Locate every Plasmodium malariae-infected red blood cell.
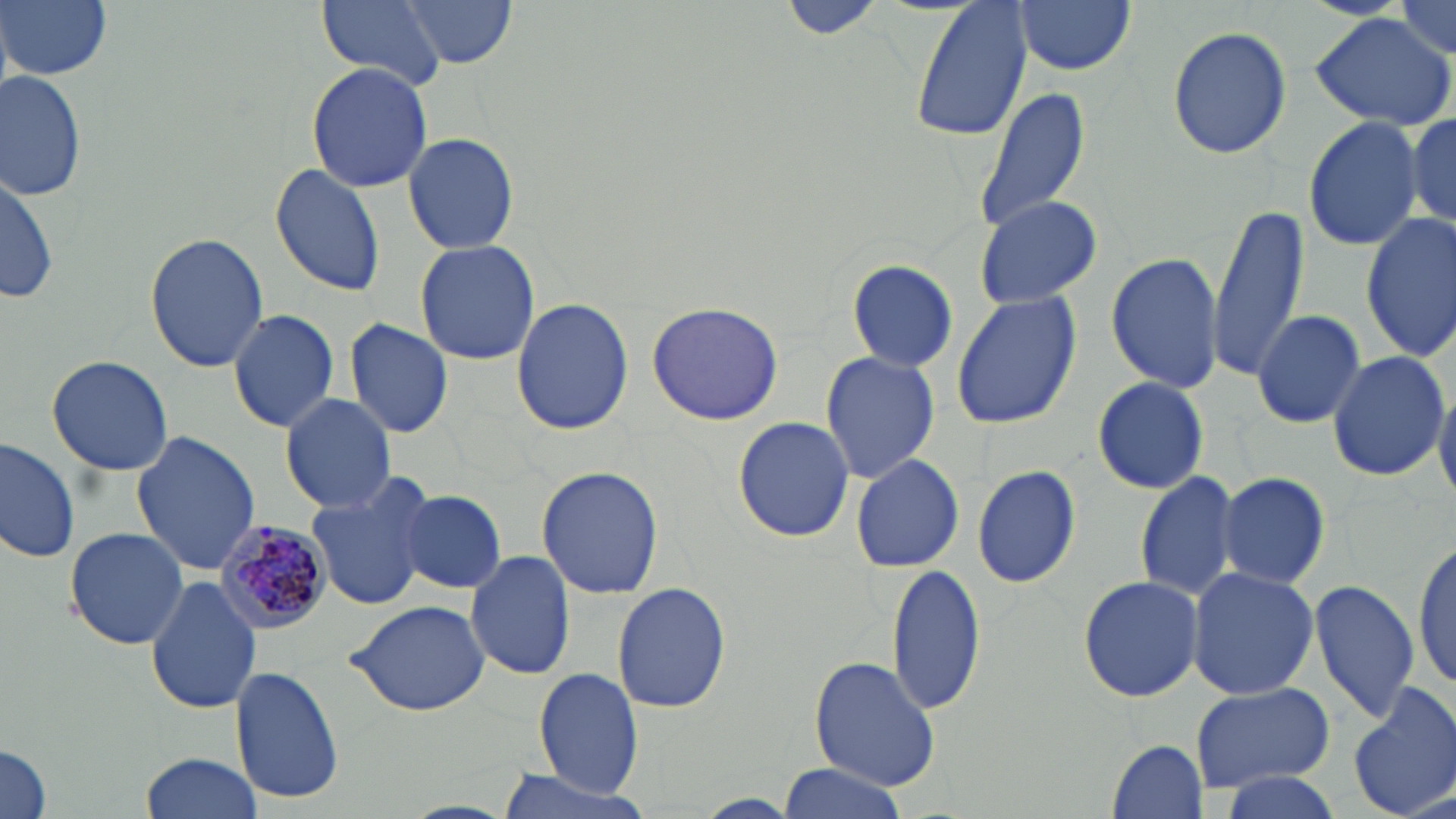

Approximate bounding boxes as (x1, y1, x2, y2) in pixels.
Plasmodium malariae-infected red blood cells: (214, 520, 336, 635).

Summary:
  - Uninfected red blood cell locations: (2, 0, 111, 80), (315, 0, 450, 89), (401, 0, 517, 69), (779, 0, 886, 41), (910, 0, 1031, 143), (1012, 0, 1136, 75), (1386, 1, 1454, 59), (1307, 13, 1456, 131), (1168, 24, 1291, 160), (306, 63, 434, 192), (1, 69, 85, 202), (974, 86, 1092, 233), (1405, 110, 1456, 231), (1303, 115, 1425, 251), (404, 134, 519, 254), (270, 161, 383, 297), (0, 169, 60, 307), (973, 195, 1102, 310), (1208, 204, 1309, 378), (1360, 211, 1456, 362), (145, 232, 269, 373), (414, 238, 540, 365), (1106, 251, 1226, 396), (846, 259, 957, 373), (950, 289, 1083, 432), (511, 298, 634, 435), (646, 302, 785, 426), (227, 308, 337, 432), (1249, 310, 1369, 429), (345, 320, 454, 438), (1327, 349, 1449, 482), (821, 350, 941, 486), (46, 354, 174, 476), (1092, 375, 1210, 496), (1433, 378, 1456, 503), (278, 392, 398, 514), (732, 416, 854, 541), (130, 429, 261, 576), (0, 434, 79, 565), (849, 452, 963, 573), (537, 465, 663, 600), (972, 465, 1081, 589), (1, 466, 113, 623), (1134, 467, 1244, 604), (304, 470, 438, 611), (1215, 470, 1331, 591), (399, 489, 506, 595), (64, 527, 188, 649), (1413, 539, 1454, 692), (465, 549, 576, 681), (885, 565, 986, 717), (1185, 567, 1320, 700), (146, 574, 262, 716), (1077, 575, 1206, 703), (1310, 578, 1420, 724), (612, 581, 732, 714), (348, 599, 492, 715), (808, 656, 942, 792), (230, 665, 345, 804), (534, 667, 644, 797), (1349, 680, 1456, 819), (1188, 682, 1334, 791), (1107, 736, 1208, 816), (0, 741, 52, 819), (140, 750, 262, 818), (778, 763, 913, 819), (491, 767, 655, 819), (1214, 768, 1351, 819)
  - Slide-level diagnosis: Plasmodium malariae
  - Modality: light microscopy
  - Image size: 1456×819 pixels
  - Field of view: one of a larger specimen
  - Magnification: 1000x
  - Preparation: thin blood smear
  - Stain: May-Grünwald-Giemsa